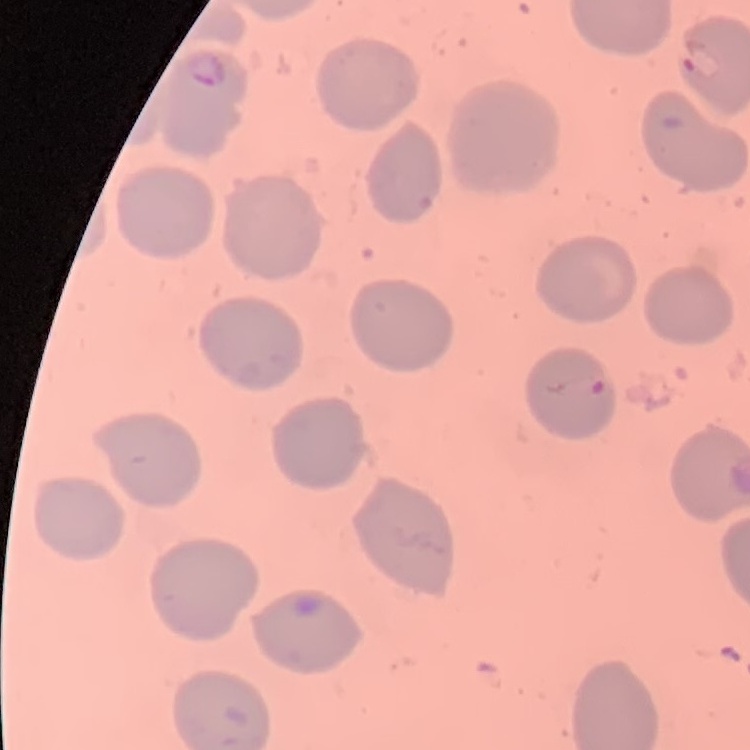 The erythrocytes exhibit no rouleaux formation. Square crop of a larger photomicrograph. Field's or Giemsa stain. Thin blood film.